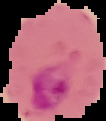 Result: malaria parasites detected. From a thin blood film. The area outside the segmented cell region is set to black. Image is 106×121 pixels.